State which parasite is depicted.
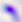
Toxoplasma gondii.

Micrograph. 400x magnification.